Locate and identify every blood parasite.
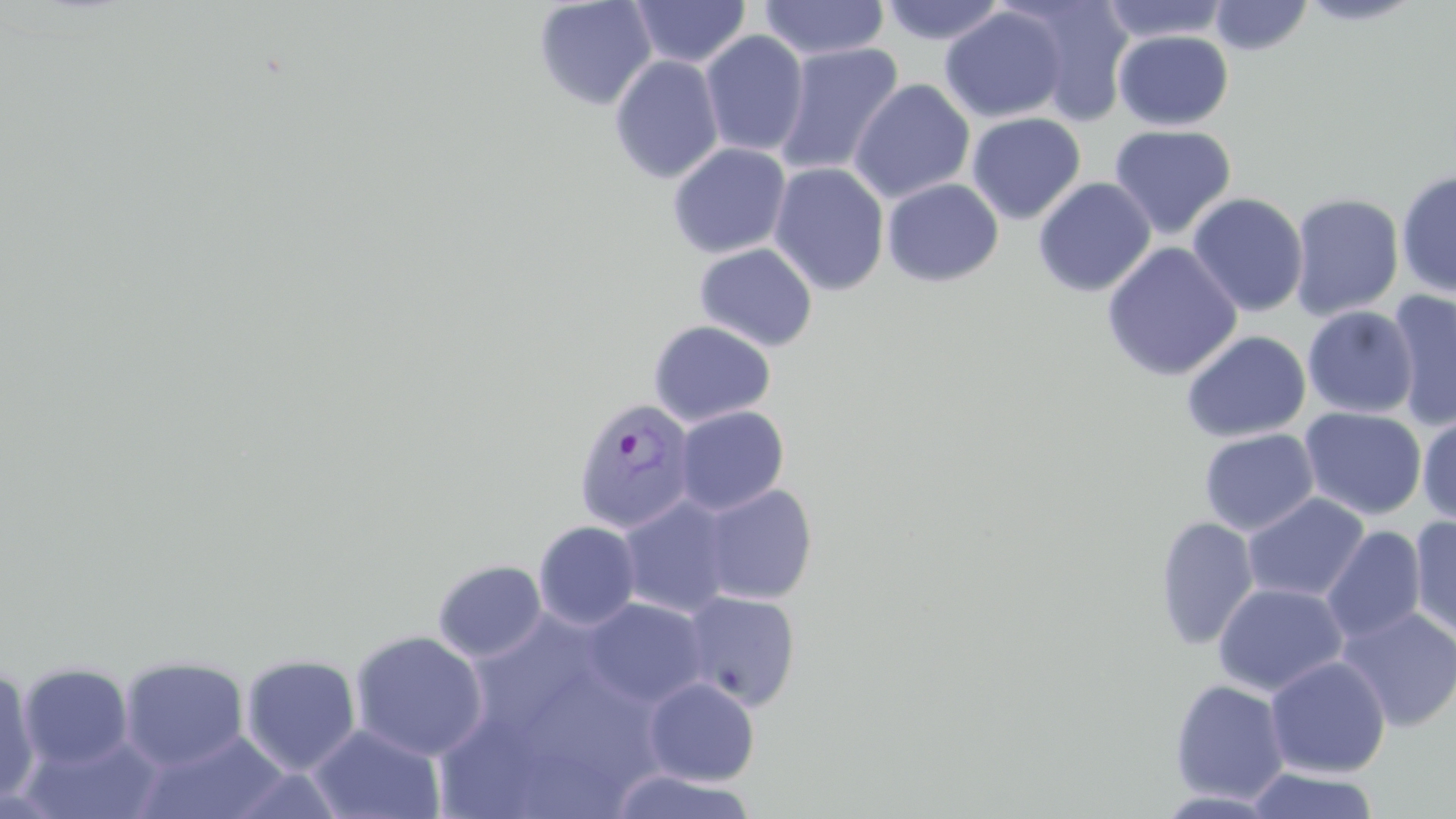

Approximate bounding boxes as (x1,y1)-(x2,y2) corner pairs in pixels.
Plasmodium vivax-infected red blood cells: (573,397)-(697,534).
No Plasmodium falciparum, Plasmodium ovale, Plasmodium malariae, Babesia divergens, or Trypanosoma brucei observed.

Summary:
  - Uninfected red blood cell locations: (630,0)-(751,68), (878,0)-(1009,45), (1098,0)-(1232,43), (1294,0)-(1429,26), (533,1)-(657,111), (758,1)-(890,61), (1010,1)-(1135,124), (1209,1)-(1313,56), (940,6)-(1067,123), (699,30)-(810,158), (1114,30)-(1234,130), (773,42)-(904,179), (609,55)-(725,184), (849,79)-(975,204), (966,113)-(1085,224), (1109,124)-(1237,240), (667,142)-(791,259), (769,162)-(890,296), (1396,168)-(1456,299), (1032,177)-(1156,297), (882,178)-(1004,287), (1187,192)-(1309,317), (1288,192)-(1405,321), (1101,242)-(1243,381), (694,243)-(818,352), (1386,290)-(1456,431), (1302,306)-(1419,418), (648,320)-(776,427), (1181,330)-(1312,443), (674,405)-(789,515), (1299,407)-(1427,520), (1417,415)-(1456,526), (1199,428)-(1319,536), (699,482)-(819,605), (1242,492)-(1370,603), (617,496)-(735,619), (1155,516)-(1260,651), (1408,516)-(1456,639), (533,520)-(642,630), (1321,526)-(1426,644), (432,558)-(548,662), (1212,582)-(1349,697), (681,590)-(802,711), (583,598)-(709,708), (1336,606)-(1456,731), (468,611)-(598,741), (349,629)-(488,761), (240,653)-(362,776), (1265,655)-(1391,778), (119,656)-(249,771), (17,662)-(133,770), (0,665)-(41,807), (511,668)-(684,780), (643,677)-(760,786), (1169,679)-(1290,804), (308,723)-(446,819), (131,729)-(293,819), (21,733)-(165,819), (496,739)-(625,819), (222,766)-(349,818), (1245,766)-(1381,818), (606,768)-(760,819)
  - Slide-level diagnosis: Plasmodium vivax
  - Modality: light microscopy
  - Image size: 1456×819 pixels
  - Magnification: 1000x
  - Preparation: thin blood film
  - Stain: May-Grünwald-Giemsa
  - Field of view: one of a larger specimen